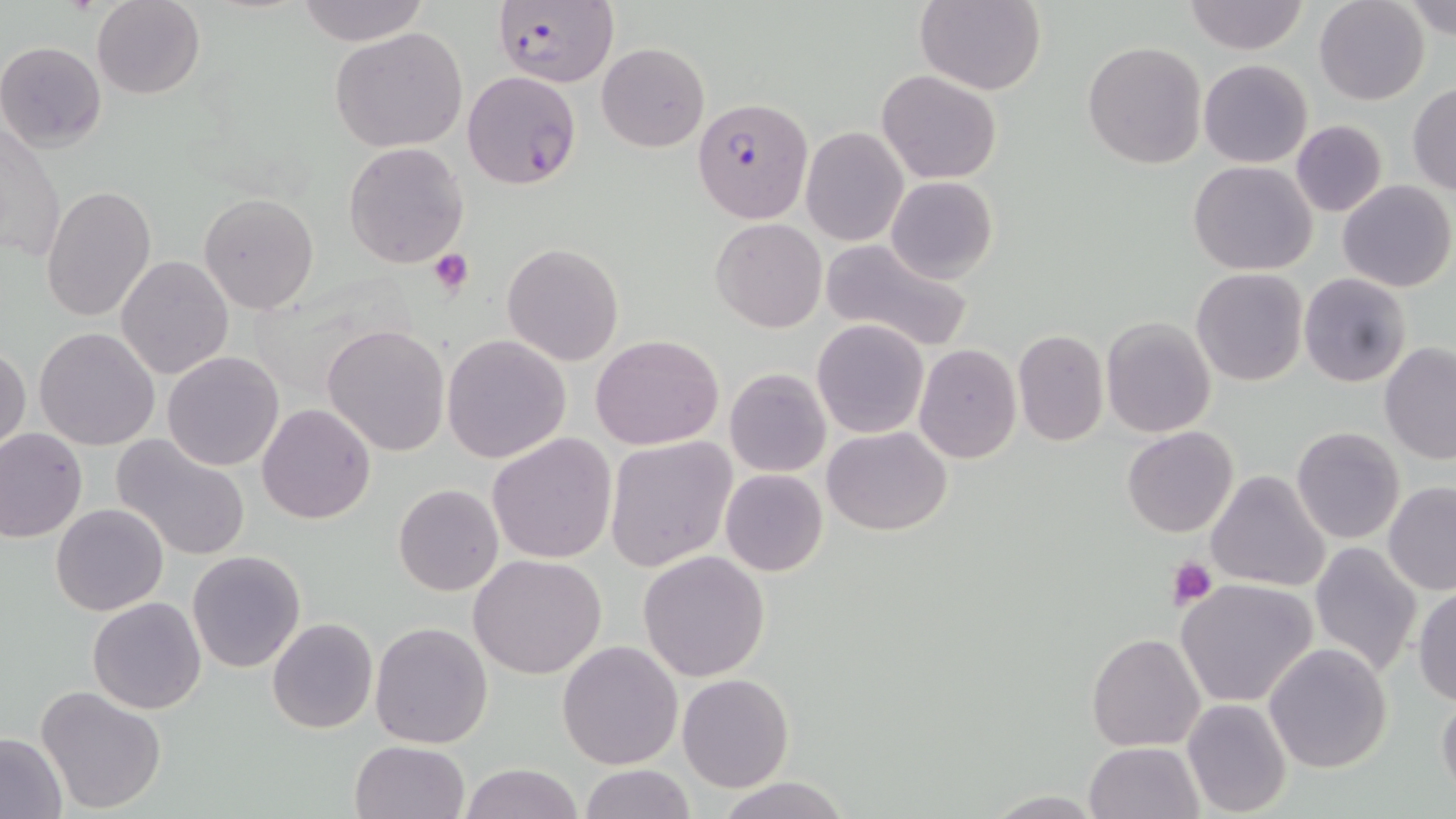

Summary:
  - Coordinate format: approximate bounding boxes as named x1/y1/x2/y2 corners in pixels
  - Uninfected red blood cell locations: (x1=92, y1=0, x2=205, y2=99), (x1=295, y1=0, x2=428, y2=46), (x1=915, y1=0, x2=1046, y2=95), (x1=1184, y1=0, x2=1309, y2=55), (x1=1403, y1=0, x2=1456, y2=41), (x1=1313, y1=1, x2=1428, y2=105), (x1=330, y1=27, x2=469, y2=154), (x1=0, y1=40, x2=107, y2=150), (x1=1082, y1=40, x2=1207, y2=170), (x1=597, y1=42, x2=709, y2=152), (x1=1198, y1=59, x2=1313, y2=168), (x1=877, y1=69, x2=1003, y2=184), (x1=462, y1=71, x2=583, y2=189), (x1=1407, y1=83, x2=1456, y2=195), (x1=1, y1=120, x2=65, y2=268), (x1=1291, y1=121, x2=1387, y2=218), (x1=800, y1=128, x2=908, y2=246), (x1=343, y1=142, x2=469, y2=266), (x1=1188, y1=160, x2=1317, y2=276), (x1=886, y1=175, x2=999, y2=283), (x1=1337, y1=179, x2=1455, y2=293), (x1=41, y1=184, x2=158, y2=322), (x1=198, y1=192, x2=320, y2=314), (x1=711, y1=218, x2=826, y2=333), (x1=819, y1=235, x2=976, y2=353), (x1=501, y1=243, x2=623, y2=366), (x1=116, y1=254, x2=234, y2=379), (x1=1191, y1=267, x2=1308, y2=386), (x1=1299, y1=273, x2=1411, y2=387), (x1=1101, y1=316, x2=1217, y2=440), (x1=812, y1=318, x2=929, y2=439), (x1=321, y1=323, x2=451, y2=457), (x1=34, y1=328, x2=160, y2=449), (x1=1012, y1=329, x2=1108, y2=446), (x1=824, y1=333, x2=1016, y2=453), (x1=441, y1=334, x2=571, y2=464), (x1=589, y1=334, x2=724, y2=451), (x1=914, y1=343, x2=1022, y2=464), (x1=1380, y1=343, x2=1456, y2=464), (x1=0, y1=345, x2=29, y2=455), (x1=162, y1=351, x2=285, y2=472), (x1=726, y1=368, x2=829, y2=477), (x1=257, y1=403, x2=376, y2=523), (x1=823, y1=426, x2=952, y2=534), (x1=1292, y1=426, x2=1405, y2=544), (x1=1123, y1=427, x2=1237, y2=537), (x1=0, y1=428, x2=87, y2=542), (x1=487, y1=433, x2=617, y2=563), (x1=111, y1=434, x2=251, y2=562), (x1=604, y1=435, x2=738, y2=571), (x1=720, y1=469, x2=828, y2=577), (x1=1206, y1=470, x2=1330, y2=592), (x1=1383, y1=482, x2=1456, y2=595), (x1=393, y1=484, x2=504, y2=597), (x1=51, y1=503, x2=170, y2=616), (x1=1308, y1=541, x2=1424, y2=676), (x1=187, y1=550, x2=307, y2=674), (x1=638, y1=550, x2=770, y2=682), (x1=468, y1=553, x2=608, y2=678), (x1=1175, y1=577, x2=1317, y2=706), (x1=1412, y1=585, x2=1456, y2=706), (x1=87, y1=597, x2=206, y2=714), (x1=267, y1=617, x2=378, y2=734), (x1=369, y1=622, x2=493, y2=748), (x1=1086, y1=633, x2=1205, y2=752), (x1=557, y1=640, x2=684, y2=770), (x1=1264, y1=642, x2=1394, y2=774), (x1=676, y1=673, x2=795, y2=792), (x1=35, y1=685, x2=168, y2=813), (x1=1436, y1=689, x2=1456, y2=799), (x1=1181, y1=698, x2=1293, y2=816), (x1=0, y1=732, x2=68, y2=817), (x1=349, y1=739, x2=472, y2=819), (x1=1084, y1=741, x2=1203, y2=819), (x1=459, y1=762, x2=584, y2=819), (x1=577, y1=764, x2=694, y2=819), (x1=714, y1=775, x2=855, y2=819)
  - Plasmodium falciparum-infected red blood cell locations: (x1=492, y1=1, x2=620, y2=87), (x1=695, y1=98, x2=810, y2=222)
  - Platelet locations: (x1=427, y1=248, x2=474, y2=296), (x1=1167, y1=556, x2=1218, y2=608)
  - Slide-level diagnosis: Plasmodium falciparum
  - Modality: optical microscopy
  - Stain: May-Grünwald-Giemsa
  - Magnification: 1000x
  - Preparation: thin blood film
  - Field of view: single
  - Image size: 1456×819 pixels